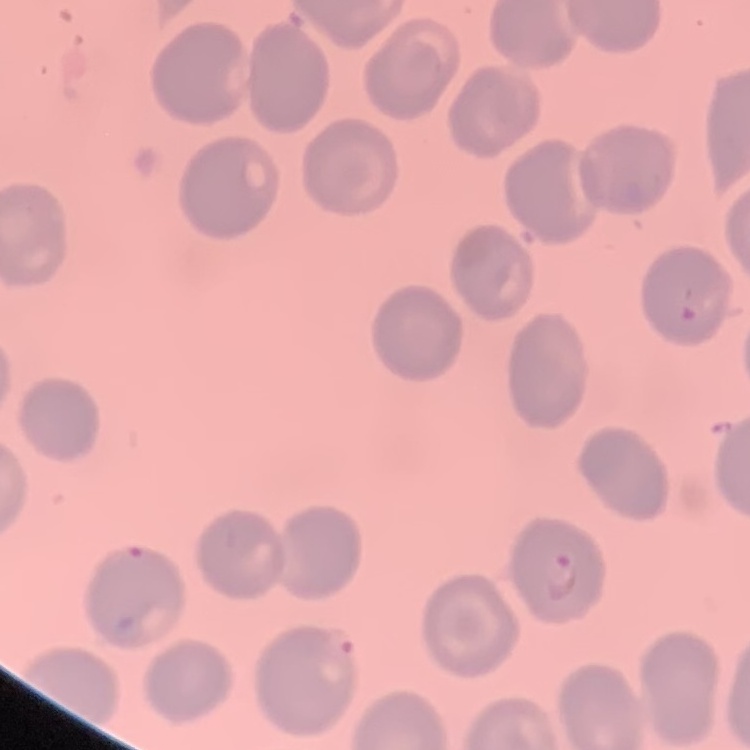

red blood cell morphology = no rouleaux formation
stain = Field's or Giemsa
image type = one tile cut from a larger photomicrograph
preparation = thin peripheral smear